Comment on the morphology of the red blood cells.
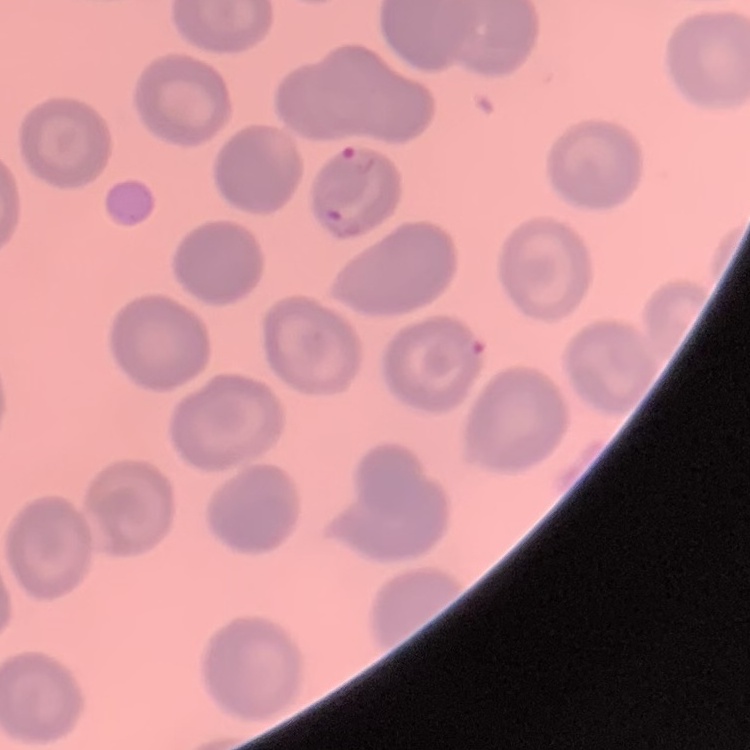

They show no rouleaux formation.

stain: Field's or Giemsa
image_type: one tile cut from a larger photomicrograph
preparation: thin peripheral smear